Name the parasite shown.
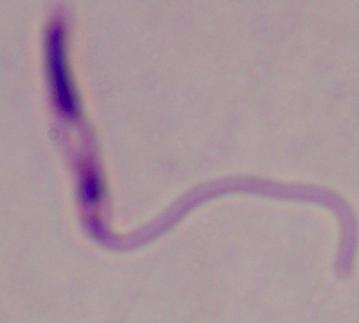

This is Leishmania.

magnification: 1000x
modality: micrograph